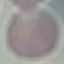
result: no malaria parasites seen
capture: smartphone through the microscope eyepiece
image_type: cell patch, automatically extracted from a larger field of view and resized to 64 × 64 pixels
preparation: thin smear
stain: Giemsa